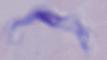 Photomicrograph. A trypanosome is shown. Captured at 1000x magnification.